Assess this cell for malaria.
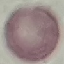

Uninfected.

Summary:
  - Image type: automatically extracted cell patch, resized to 64 × 64 pixels
  - Preparation: thin blood smear
  - Stain: Giemsa
  - Capture: smartphone camera at the microscope eyepiece